Assess for Plasmodium parasites.
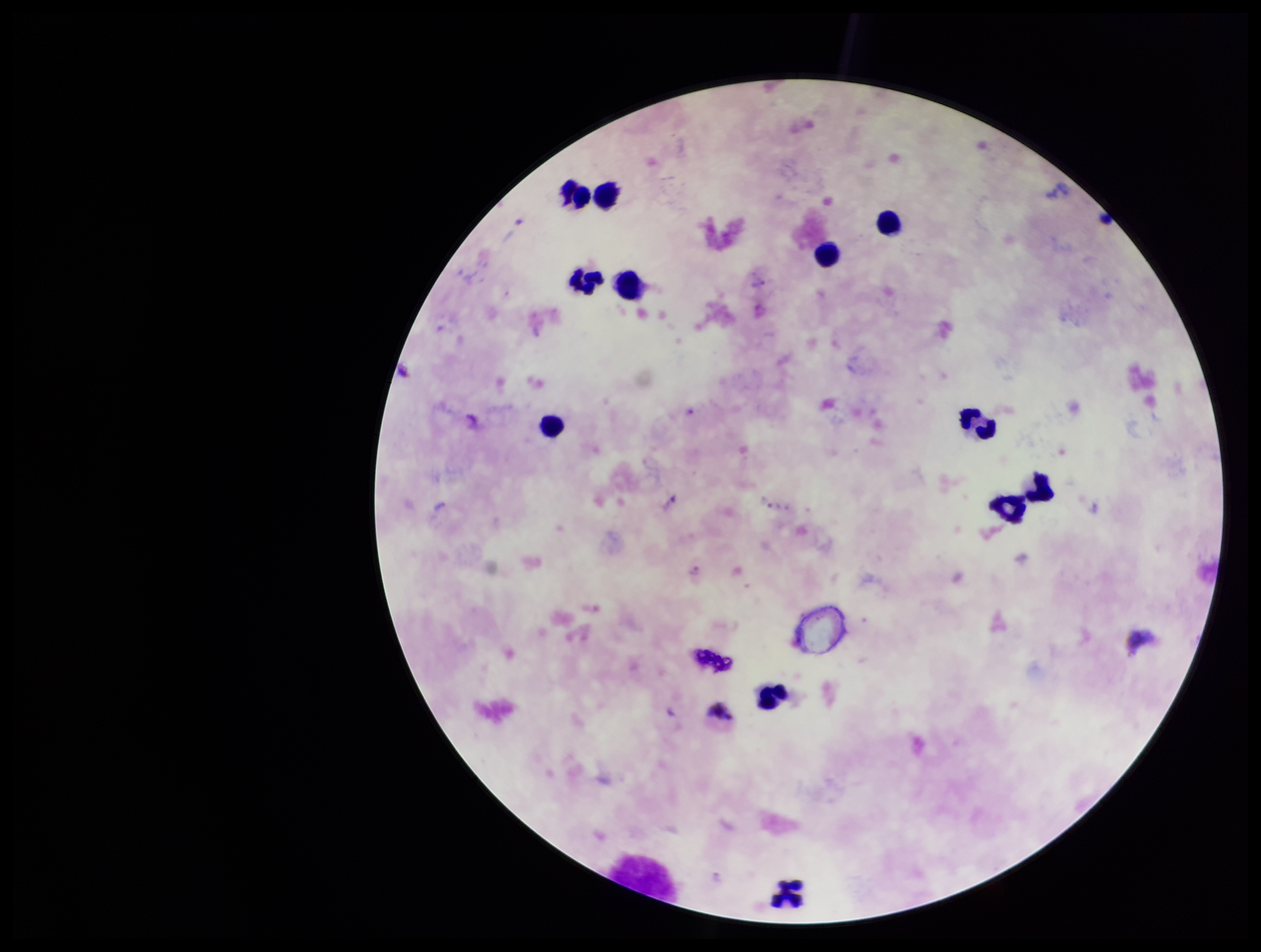

None identified.

species_reported_for_this_patient: Plasmodium vivax
preparation: thick
image_size: 1261×952 pixels
patient_malaria_status: infected
leukocyte_count: 12
stain: Giemsa
field_of_view: single
capture: smartphone photograph through the microscope eyepiece
parasite_count: 0